Name the parasite shown.
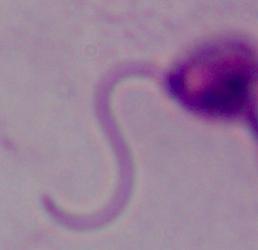

Leishmania.

Summary:
  - Magnification: 1000x
  - Modality: micrograph